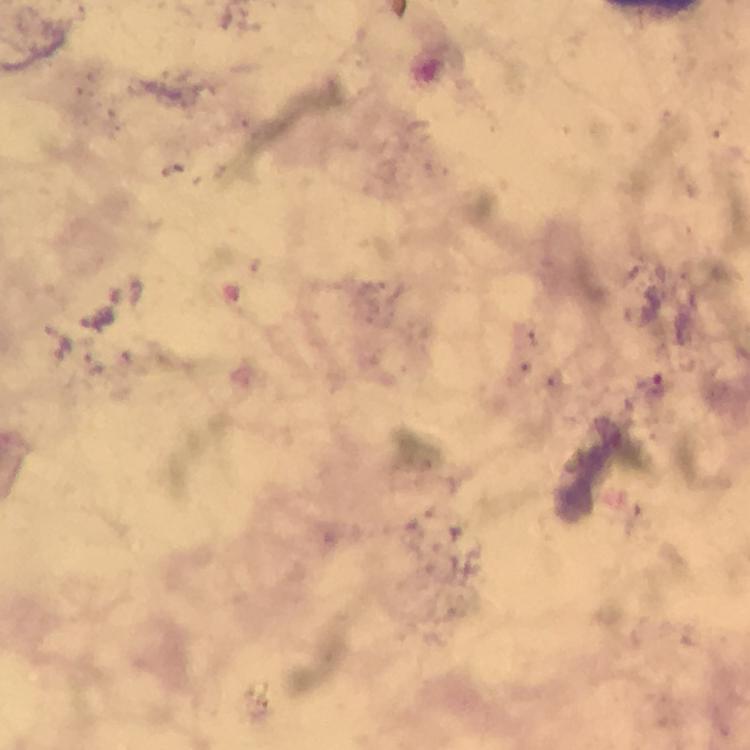
Approximate centers as {x, y} in pixels.
Summary:
  - Plasmodium parasite locations: {660, 386}
  - Immersion oil: used
  - Capture: smartphone photograph through a microscope
  - Magnification: 100x
  - Image size: 750×750 pixels
  - Cropped from: a single field of view
  - Context: from a diagnostic examination for malaria
  - Preparation: thick blood smear
  - Stain: Giemsa